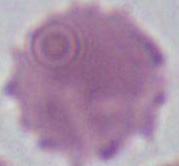
Captured at 1000x magnification. Micrograph. An erythrocyte is seen.